Locate every Plasmodium vivax-infected red blood cell.
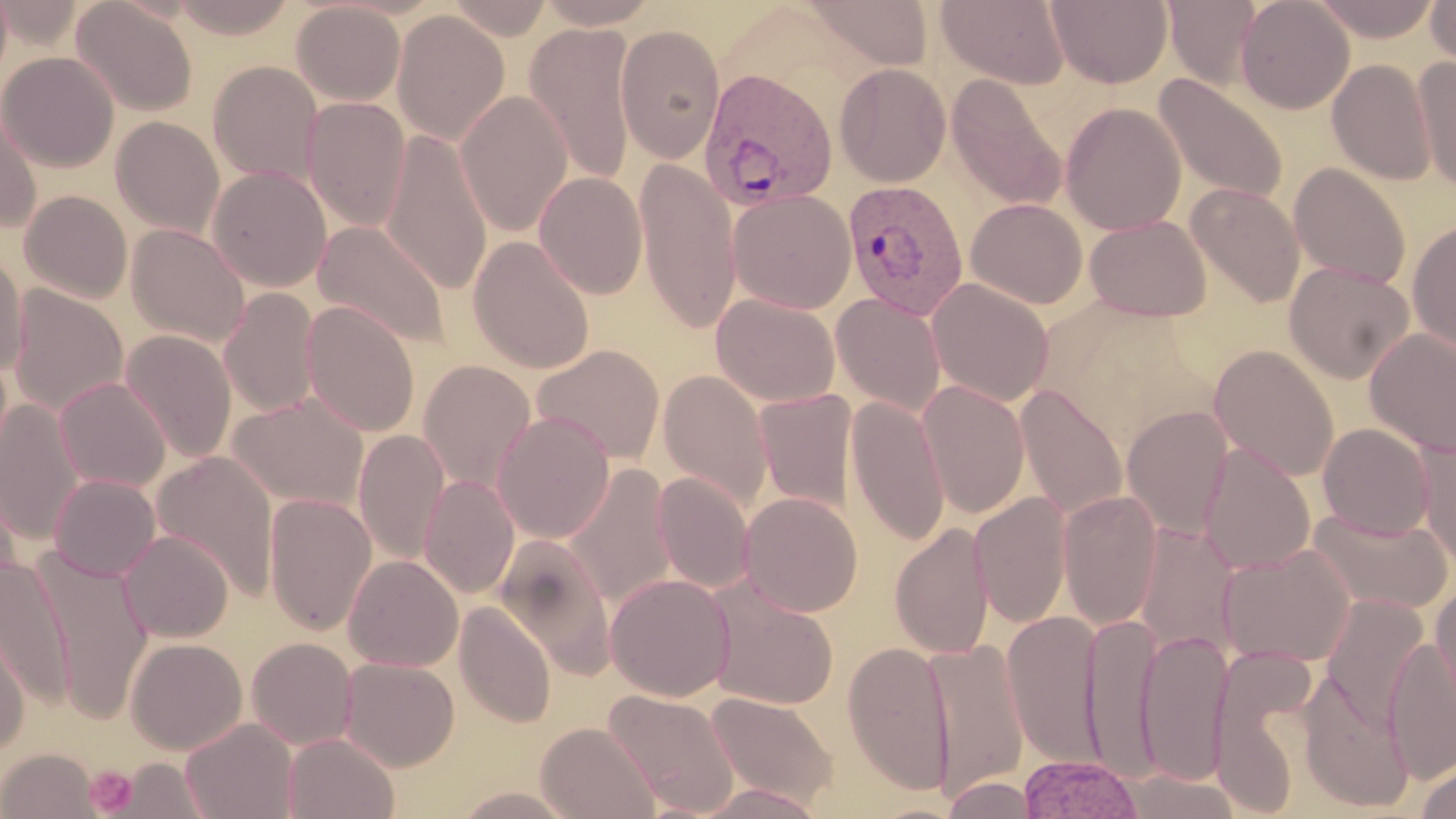
Approximate bounding boxes as named x1/y1/x2/y2 corners in pixels.
Plasmodium vivax-infected red blood cells: (x1=698, y1=68, x2=839, y2=212), (x1=842, y1=179, x2=969, y2=319).

Summary:
  - Uninfected red blood cell locations: (x1=70, y1=0, x2=198, y2=117), (x1=170, y1=0, x2=297, y2=39), (x1=446, y1=0, x2=554, y2=40), (x1=534, y1=0, x2=661, y2=28), (x1=936, y1=0, x2=1069, y2=88), (x1=1046, y1=0, x2=1173, y2=89), (x1=1163, y1=0, x2=1263, y2=90), (x1=1236, y1=0, x2=1355, y2=114), (x1=1310, y1=0, x2=1442, y2=42), (x1=1426, y1=0, x2=1456, y2=69), (x1=798, y1=1, x2=935, y2=71), (x1=292, y1=2, x2=406, y2=106), (x1=392, y1=9, x2=510, y2=146), (x1=525, y1=21, x2=638, y2=186), (x1=615, y1=23, x2=725, y2=164), (x1=1, y1=52, x2=119, y2=172), (x1=1412, y1=56, x2=1456, y2=193), (x1=1328, y1=59, x2=1436, y2=185), (x1=207, y1=60, x2=323, y2=186), (x1=834, y1=63, x2=951, y2=187), (x1=945, y1=74, x2=1068, y2=212), (x1=1152, y1=74, x2=1288, y2=205), (x1=455, y1=90, x2=572, y2=236), (x1=302, y1=97, x2=411, y2=233), (x1=1060, y1=102, x2=1186, y2=236), (x1=0, y1=103, x2=42, y2=232), (x1=110, y1=116, x2=225, y2=239), (x1=380, y1=129, x2=493, y2=296), (x1=633, y1=158, x2=740, y2=334), (x1=1288, y1=163, x2=1410, y2=288), (x1=207, y1=166, x2=332, y2=292), (x1=534, y1=171, x2=648, y2=298), (x1=1186, y1=184, x2=1304, y2=309), (x1=19, y1=190, x2=133, y2=304), (x1=728, y1=190, x2=857, y2=314), (x1=965, y1=198, x2=1088, y2=309), (x1=1084, y1=215, x2=1211, y2=321), (x1=1407, y1=219, x2=1456, y2=354), (x1=312, y1=220, x2=450, y2=351), (x1=126, y1=224, x2=250, y2=347), (x1=468, y1=236, x2=595, y2=374), (x1=0, y1=250, x2=29, y2=378), (x1=1284, y1=261, x2=1414, y2=383), (x1=927, y1=278, x2=1054, y2=407), (x1=7, y1=284, x2=128, y2=419), (x1=218, y1=289, x2=321, y2=418), (x1=711, y1=293, x2=841, y2=407), (x1=831, y1=293, x2=946, y2=418), (x1=301, y1=301, x2=420, y2=437), (x1=1365, y1=328, x2=1456, y2=457), (x1=119, y1=330, x2=237, y2=466), (x1=531, y1=344, x2=666, y2=465), (x1=1209, y1=344, x2=1339, y2=481), (x1=418, y1=359, x2=537, y2=493), (x1=657, y1=369, x2=773, y2=513), (x1=54, y1=377, x2=171, y2=493), (x1=917, y1=380, x2=1031, y2=519), (x1=1015, y1=383, x2=1127, y2=521), (x1=753, y1=388, x2=858, y2=516), (x1=228, y1=393, x2=369, y2=511), (x1=846, y1=395, x2=950, y2=547), (x1=0, y1=399, x2=84, y2=545), (x1=1122, y1=405, x2=1234, y2=538), (x1=492, y1=412, x2=614, y2=543), (x1=1318, y1=423, x2=1435, y2=541), (x1=353, y1=429, x2=450, y2=564), (x1=1417, y1=436, x2=1456, y2=576), (x1=1198, y1=442, x2=1316, y2=575), (x1=151, y1=450, x2=280, y2=601), (x1=562, y1=463, x2=677, y2=611), (x1=0, y1=471, x2=24, y2=603), (x1=653, y1=473, x2=754, y2=593), (x1=49, y1=474, x2=160, y2=581), (x1=419, y1=475, x2=519, y2=599), (x1=1058, y1=490, x2=1163, y2=629), (x1=739, y1=491, x2=863, y2=617), (x1=970, y1=491, x2=1072, y2=630), (x1=264, y1=493, x2=377, y2=636), (x1=1307, y1=506, x2=1454, y2=616), (x1=890, y1=522, x2=994, y2=660), (x1=1132, y1=522, x2=1241, y2=658), (x1=118, y1=530, x2=234, y2=642), (x1=494, y1=534, x2=618, y2=680), (x1=1217, y1=544, x2=1356, y2=669), (x1=40, y1=554, x2=152, y2=723), (x1=343, y1=554, x2=463, y2=672), (x1=0, y1=556, x2=75, y2=710), (x1=605, y1=573, x2=736, y2=702), (x1=705, y1=575, x2=840, y2=711), (x1=1431, y1=580, x2=1456, y2=717), (x1=1320, y1=594, x2=1430, y2=732), (x1=454, y1=601, x2=556, y2=728), (x1=1002, y1=608, x2=1106, y2=772), (x1=1082, y1=612, x2=1162, y2=781), (x1=1, y1=619, x2=32, y2=754), (x1=1135, y1=627, x2=1234, y2=787), (x1=1383, y1=636, x2=1456, y2=783), (x1=125, y1=637, x2=247, y2=754), (x1=246, y1=637, x2=358, y2=750), (x1=923, y1=638, x2=1030, y2=800), (x1=843, y1=640, x2=955, y2=794), (x1=1208, y1=646, x2=1322, y2=816), (x1=339, y1=657, x2=459, y2=771), (x1=1296, y1=670, x2=1416, y2=812), (x1=603, y1=688, x2=740, y2=816), (x1=706, y1=691, x2=839, y2=809), (x1=180, y1=717, x2=299, y2=819), (x1=535, y1=722, x2=660, y2=819), (x1=283, y1=733, x2=400, y2=819), (x1=1, y1=747, x2=100, y2=819), (x1=1018, y1=753, x2=1144, y2=818), (x1=110, y1=758, x2=213, y2=818), (x1=1413, y1=758, x2=1455, y2=819), (x1=1112, y1=768, x2=1245, y2=818), (x1=942, y1=776, x2=1042, y2=819), (x1=691, y1=783, x2=831, y2=819), (x1=447, y1=786, x2=585, y2=818)
  - Platelet locations: (x1=84, y1=764, x2=138, y2=816)
  - Slide-level diagnosis: Plasmodium vivax
  - Modality: optical microscopy
  - Image size: 1456×819 pixels
  - Preparation: thin blood smear
  - Stain: May-Grünwald-Giemsa
  - Field of view: one of a larger specimen
  - Magnification: 1000x